Identify the blood parasite species.
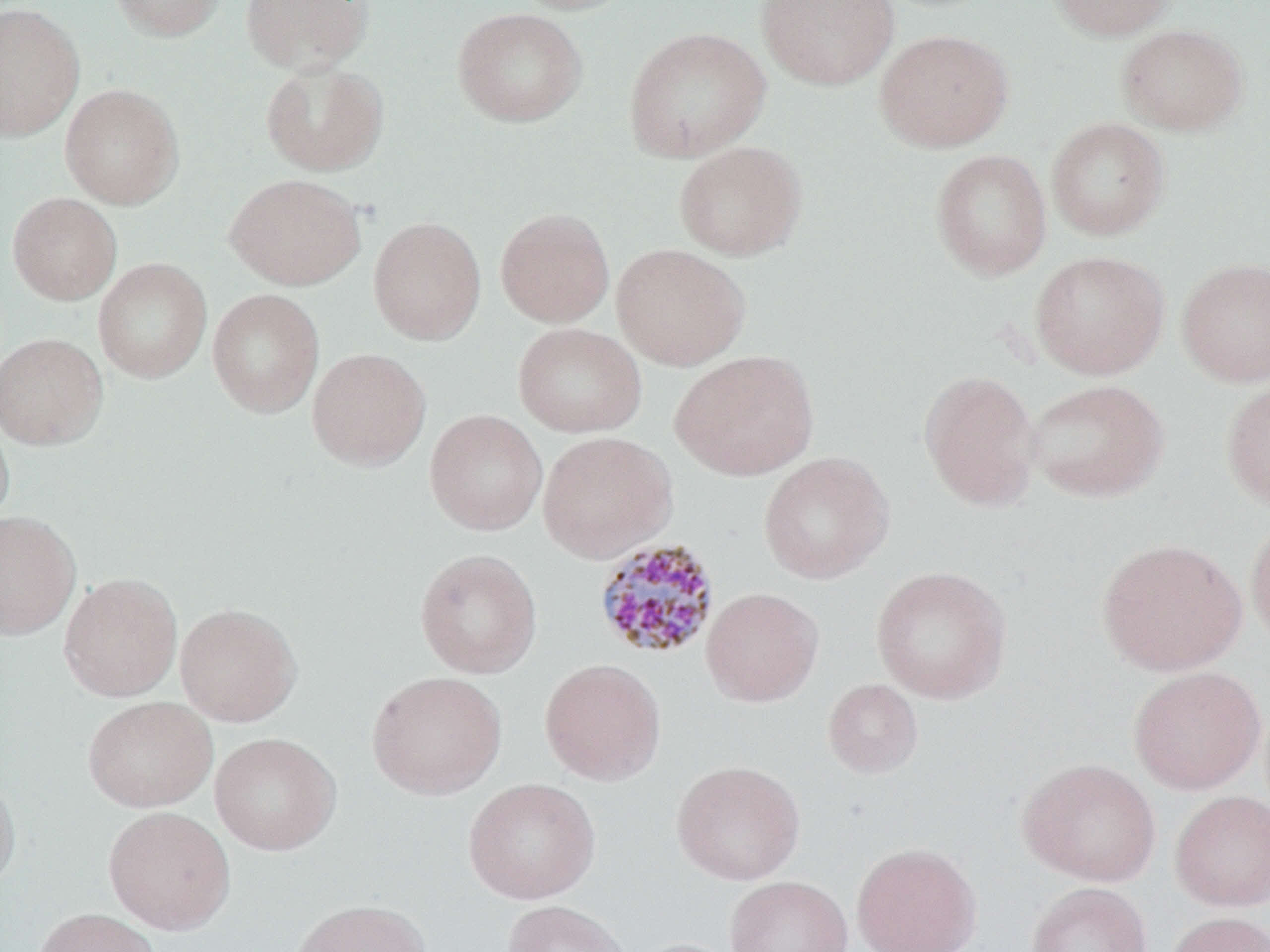

Plasmodium malariae.

modality = optical microscopy
stain = May-Grünwald-Giemsa
field of view = single
Plasmodium malariae-infected red blood cell locations = approximate bounding boxes as named x1/y1/x2/y2 corners in pixels: (x1=593, y1=537, x2=722, y2=661)
image size = 1270×952 pixels
preparation = thin blood film
uninfected red blood cell locations = approximate bounding boxes as named x1/y1/x2/y2 corners in pixels: (x1=107, y1=0, x2=226, y2=42), (x1=240, y1=0, x2=373, y2=75), (x1=508, y1=0, x2=641, y2=15), (x1=756, y1=0, x2=899, y2=90), (x1=1046, y1=0, x2=1177, y2=41), (x1=0, y1=2, x2=84, y2=142), (x1=452, y1=7, x2=587, y2=127), (x1=1116, y1=23, x2=1249, y2=136), (x1=623, y1=26, x2=770, y2=162), (x1=874, y1=28, x2=1015, y2=153), (x1=260, y1=60, x2=389, y2=176), (x1=59, y1=83, x2=185, y2=210), (x1=1046, y1=117, x2=1170, y2=240), (x1=673, y1=141, x2=807, y2=261), (x1=930, y1=148, x2=1052, y2=281), (x1=224, y1=173, x2=366, y2=291), (x1=7, y1=192, x2=122, y2=305), (x1=495, y1=207, x2=615, y2=328), (x1=368, y1=216, x2=486, y2=345), (x1=611, y1=243, x2=751, y2=370), (x1=1029, y1=250, x2=1169, y2=380), (x1=1175, y1=256, x2=1270, y2=387), (x1=93, y1=257, x2=213, y2=383), (x1=207, y1=288, x2=325, y2=418), (x1=512, y1=322, x2=648, y2=438), (x1=0, y1=332, x2=108, y2=450), (x1=306, y1=347, x2=431, y2=471), (x1=670, y1=350, x2=819, y2=481), (x1=918, y1=369, x2=1041, y2=512), (x1=1024, y1=378, x2=1169, y2=502), (x1=1221, y1=378, x2=1270, y2=511), (x1=0, y1=408, x2=15, y2=533), (x1=425, y1=409, x2=548, y2=535), (x1=537, y1=430, x2=677, y2=564), (x1=757, y1=451, x2=895, y2=585), (x1=0, y1=510, x2=81, y2=640), (x1=1246, y1=515, x2=1270, y2=650), (x1=1095, y1=537, x2=1247, y2=676), (x1=414, y1=548, x2=542, y2=679), (x1=870, y1=566, x2=1012, y2=704), (x1=59, y1=572, x2=183, y2=702), (x1=700, y1=587, x2=824, y2=707), (x1=174, y1=602, x2=302, y2=727), (x1=540, y1=658, x2=666, y2=785), (x1=1128, y1=665, x2=1266, y2=794), (x1=366, y1=670, x2=507, y2=800), (x1=823, y1=678, x2=923, y2=779), (x1=82, y1=696, x2=218, y2=813), (x1=209, y1=732, x2=342, y2=856), (x1=1017, y1=757, x2=1160, y2=886), (x1=671, y1=759, x2=805, y2=885), (x1=0, y1=771, x2=21, y2=895), (x1=463, y1=777, x2=601, y2=904), (x1=1169, y1=790, x2=1270, y2=911), (x1=103, y1=806, x2=236, y2=934), (x1=851, y1=842, x2=982, y2=952), (x1=724, y1=875, x2=853, y2=952), (x1=1026, y1=881, x2=1152, y2=952), (x1=289, y1=899, x2=431, y2=952), (x1=502, y1=899, x2=632, y2=952), (x1=31, y1=907, x2=161, y2=952), (x1=1163, y1=910, x2=1270, y2=952), (x1=628, y1=937, x2=744, y2=952)
magnification = 1000x